Identify the parasite.
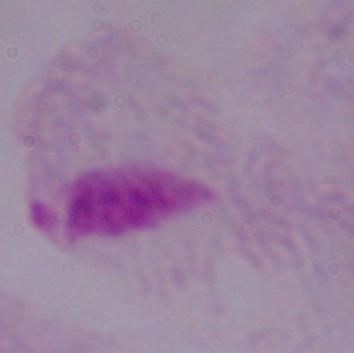
A trichomonad.

Summary:
  - Modality: micrograph
  - Magnification: 1000x